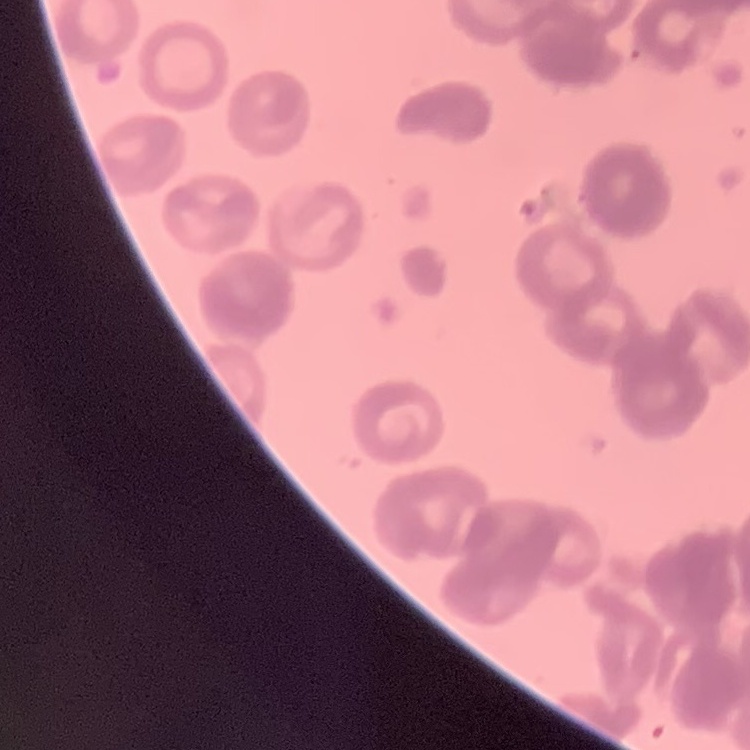
{
  "red_blood_cell_morphology": "rouleaux formation",
  "image_type": "one tile cut from a larger photomicrograph",
  "preparation": "thin peripheral smear",
  "stain": "Field's or Giemsa"
}